Assess this cell for malaria.
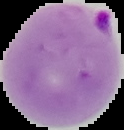

It is parasitized.

Segmented cell region on a black background. From a thin blood smear. Image is 124×130 pixels.